State which parasite is depicted.
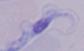
A trypanosome.

Photomicrograph. Captured at 1000x magnification.